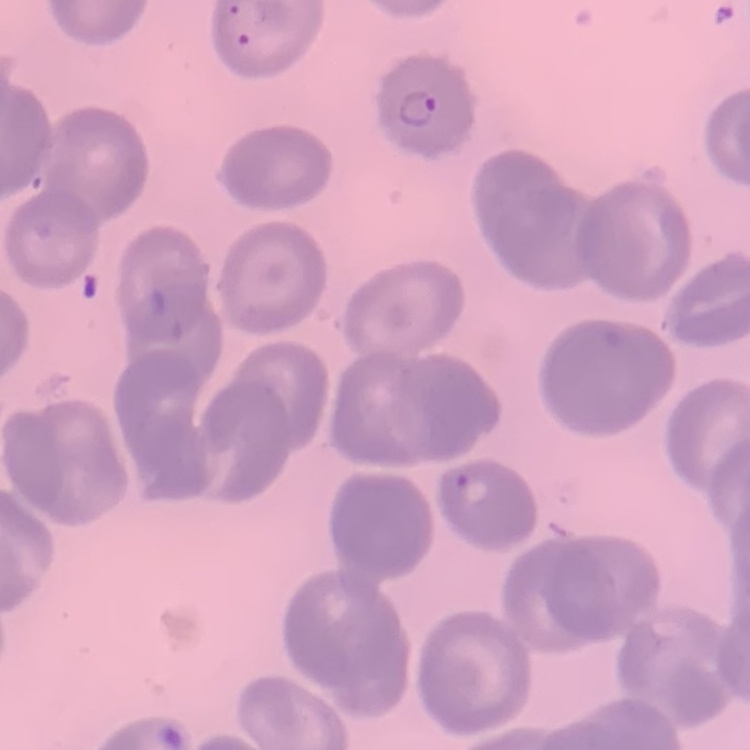
{
  "erythrocyte_morphology": "no rouleaux formation",
  "preparation": "thin blood smear",
  "stain": "Field's or Giemsa",
  "image_type": "square crop of a larger photomicrograph"
}